Assess this cell for malaria.
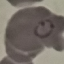
It is parasitized.

Giemsa stain. Thin smear of blood. Photographed with a smartphone camera at the microscope eyepiece. Cell patch, automatically extracted from a larger field of view and resized to 64 × 64 pixels.